Comment on the morphology of the erythrocytes.
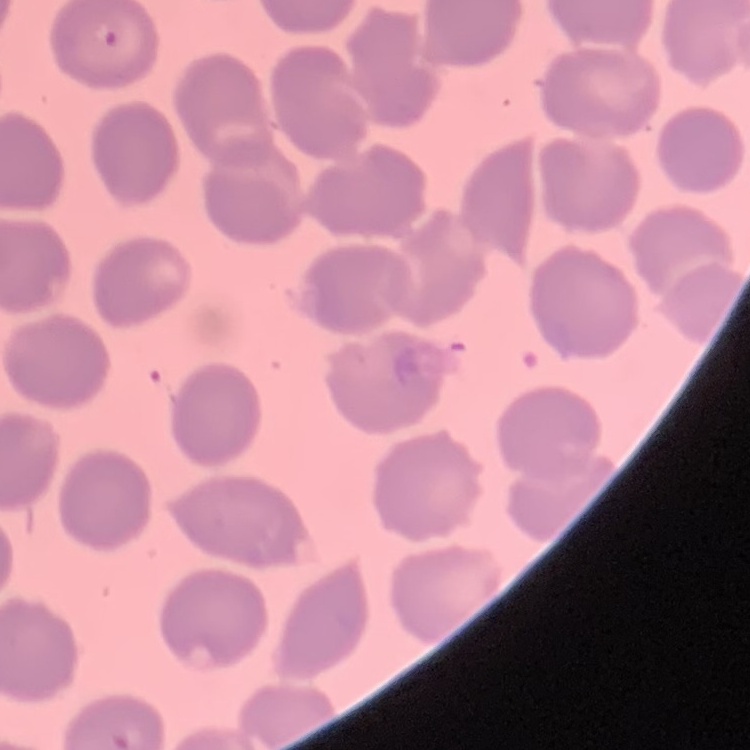

No rouleaux formation.

{
  "stain": "Field's or Giemsa",
  "image_type": "one tile cut from a larger photomicrograph",
  "preparation": "thin blood film"
}